Name the blood parasite species.
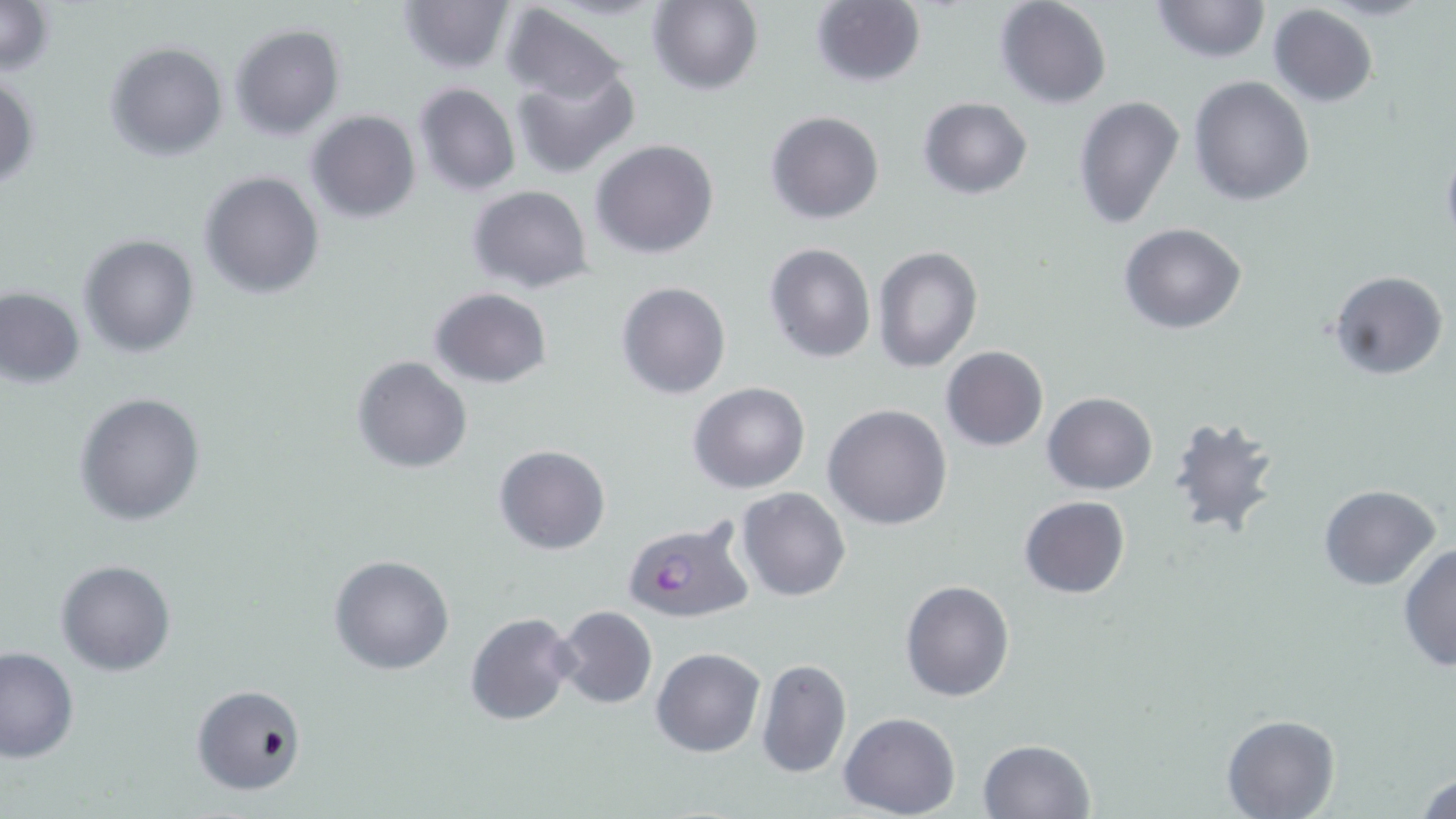
Plasmodium falciparum.

Approximate bounding boxes as (x1, y1, x2, y2) in pixels. Uninfected red blood cell locations: (0, 0, 54, 77), (396, 0, 515, 75), (1148, 0, 1271, 64), (645, 1, 763, 94), (810, 1, 926, 89), (993, 1, 1112, 109), (1268, 4, 1379, 107), (501, 5, 628, 106), (229, 23, 344, 141), (103, 41, 228, 161), (510, 66, 640, 179), (0, 73, 39, 190), (1188, 76, 1316, 207), (412, 82, 521, 198), (1074, 94, 1184, 232), (918, 97, 1033, 200), (765, 109, 885, 224), (304, 110, 420, 225), (590, 138, 720, 259), (1439, 139, 1456, 252), (198, 170, 325, 299), (466, 184, 594, 294), (1119, 222, 1246, 334), (78, 234, 198, 357), (763, 242, 876, 363), (872, 245, 983, 372), (1329, 271, 1447, 382), (615, 281, 731, 400), (1, 286, 86, 389), (429, 286, 552, 388), (941, 346, 1048, 451), (352, 356, 473, 475), (688, 382, 811, 495), (73, 391, 207, 527), (1042, 392, 1157, 493), (823, 404, 953, 531), (1166, 416, 1281, 538), (494, 445, 610, 555), (1318, 484, 1441, 589), (735, 487, 851, 601), (1018, 496, 1131, 600), (1397, 542, 1456, 673), (330, 554, 456, 675), (56, 558, 176, 675), (900, 580, 1015, 701), (552, 605, 657, 710), (464, 612, 580, 727), (0, 645, 79, 762), (651, 647, 766, 757), (756, 658, 852, 779), (190, 684, 306, 797), (839, 712, 960, 818), (1222, 712, 1341, 817), (978, 739, 1095, 819), (1413, 766, 1456, 819). Plasmodium falciparum-infected red blood cell locations: (619, 514, 754, 625). Optical microscopy. Image is 1456×819 pixels. Captured at 1000x magnification. Thin blood smear. Single field of view. May-Grünwald-Giemsa-stained preparation.